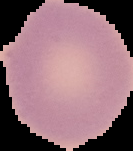

image type = cell region segmented out of the field of view; surrounding area masked to black
image size = 133×151 pixels
malaria status = uninfected
preparation = thin blood film